State which parasite is depicted.
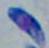
This is Toxoplasma gondii.

Summary:
  - Magnification: 1000x
  - Modality: micrograph